Locate every blood parasite and identify its species.
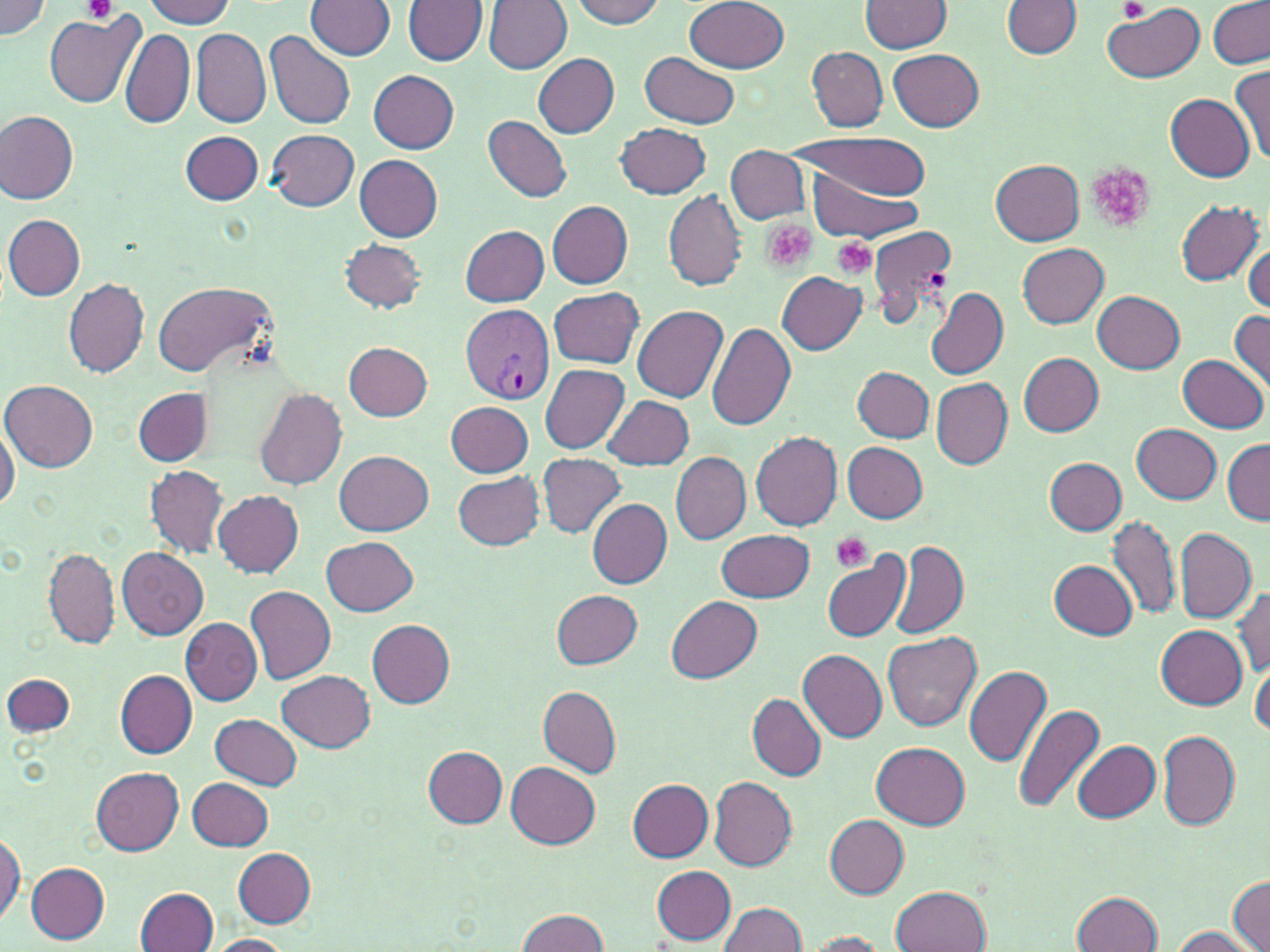

Approximate bounding boxes as (x1,y1)-(x2,y2) corner pairs in pixels.
Plasmodium vivax-infected red blood cells: (460,304)-(555,404).
No Plasmodium falciparum, Plasmodium ovale, Plasmodium malariae, Babesia divergens, or Trypanosoma brucei observed.

Platelet locations: (84,0)-(117,24), (1120,0)-(1150,22), (1086,163)-(1157,233), (761,220)-(815,274), (833,237)-(878,280), (924,268)-(946,291), (829,531)-(873,573). Uninfected red blood cell locations: (142,0)-(236,28), (306,0)-(396,60), (485,0)-(573,73), (569,0)-(666,29), (863,0)-(953,53), (1208,0)-(1270,69), (1,1)-(53,40), (403,1)-(488,66), (685,1)-(789,74), (1003,2)-(1083,57), (1103,4)-(1205,83), (45,13)-(140,108), (119,25)-(195,131), (190,28)-(270,128), (264,30)-(357,131), (805,47)-(889,132), (888,48)-(984,131), (640,52)-(740,128), (533,54)-(619,137), (1230,64)-(1270,163), (369,70)-(460,153), (1166,94)-(1256,181), (0,109)-(78,203), (483,115)-(573,202), (616,123)-(712,199), (267,129)-(359,210), (182,131)-(263,204), (792,131)-(933,202), (725,145)-(812,224), (355,154)-(443,242), (992,159)-(1083,244), (801,168)-(924,245), (663,190)-(748,291), (547,201)-(634,289), (1176,201)-(1264,285), (3,214)-(86,301), (865,223)-(958,327), (459,225)-(549,305), (341,240)-(428,312), (1017,243)-(1109,329), (1244,243)-(1270,314), (777,272)-(865,354), (63,278)-(149,377), (152,280)-(275,377), (549,287)-(644,368), (927,287)-(1008,380), (1092,289)-(1186,372), (631,304)-(728,402), (1229,310)-(1270,391), (706,320)-(797,431), (344,342)-(432,420), (1017,352)-(1104,434), (1179,354)-(1268,433), (539,365)-(629,453), (852,366)-(934,443), (932,378)-(1013,469), (2,379)-(97,472), (134,387)-(211,466), (253,388)-(347,489), (602,395)-(694,470), (445,401)-(533,477), (0,414)-(19,515), (1132,423)-(1221,504), (751,432)-(844,530), (1222,439)-(1269,525), (842,442)-(928,523), (334,451)-(433,536), (669,451)-(752,544), (537,452)-(626,538), (1045,457)-(1126,536), (147,465)-(227,558), (453,471)-(544,550), (213,489)-(305,577), (588,499)-(672,590), (1109,514)-(1180,618), (1175,528)-(1256,625), (717,529)-(813,601), (322,536)-(418,616), (890,540)-(967,639), (44,547)-(119,649), (118,547)-(209,640), (820,550)-(912,643), (1049,559)-(1138,639), (245,586)-(336,686), (1233,587)-(1270,677), (552,590)-(643,669), (666,596)-(762,684), (180,617)-(261,705), (366,619)-(456,706), (1155,625)-(1247,708), (883,630)-(981,732), (799,650)-(888,742), (964,666)-(1051,769), (1251,666)-(1269,737), (114,669)-(197,757), (278,670)-(376,751), (3,673)-(75,734), (538,686)-(621,779), (748,693)-(827,781), (1014,703)-(1106,816), (211,714)-(303,789), (1158,731)-(1240,831), (871,741)-(970,830), (1073,741)-(1161,822), (424,746)-(508,828), (505,762)-(600,848), (91,767)-(184,855), (707,774)-(797,870), (188,778)-(274,849), (628,780)-(714,861), (825,814)-(909,898), (0,828)-(24,927), (233,847)-(318,926), (26,862)-(110,943), (651,864)-(737,943), (1229,876)-(1269,951), (892,886)-(990,952), (137,887)-(219,952), (1073,891)-(1162,952), (720,903)-(810,952), (516,908)-(609,952), (1169,927)-(1257,951), (801,931)-(889,950), (201,934)-(295,952). Slide-level diagnosis: Plasmodium vivax. Light microscopy. May-Grünwald-Giemsa stain. One field of a larger specimen. Image is 1270×952 pixels. Thin blood smear. Captured at 1000x magnification.